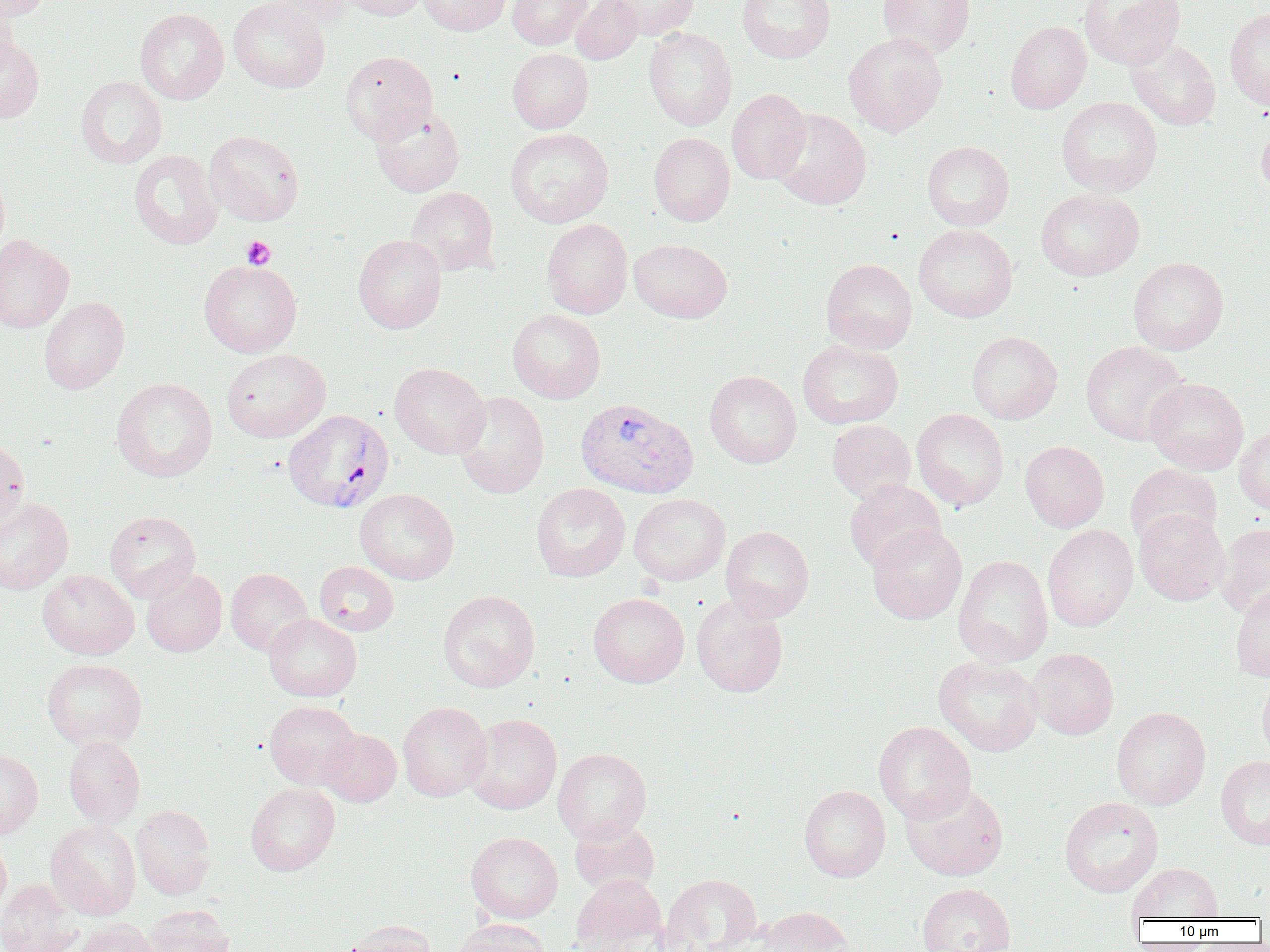

slide_level_diagnosis: Plasmodium vivax
magnification: 1000x
platelet_locations: 'approximate bounding boxes as (x1,y1)-(x2,y2) corner pairs in pixels: (242,235)-(276,270)'
modality: light microscopy
image_size: 1270×952 pixels
preparation: thin blood film
field_of_view: one of a larger specimen
uninfected_red_blood_cell_locations: 'approximate bounding boxes as (x1,y1)-(x2,y2) corner pairs in pixels: (0,0)-(50,20), (229,0)-(330,93), (262,0)-(356,23), (338,0)-(426,21), (419,0)-(510,36), (507,0)-(591,50), (570,0)-(643,65), (612,0)-(699,39), (737,0)-(835,63), (877,0)-(976,58), (1079,0)-(1186,69), (0,3)-(20,79), (1224,7)-(1270,109), (135,8)-(229,104), (1005,21)-(1092,114), (643,27)-(737,130), (843,32)-(947,136), (0,36)-(45,124), (1126,39)-(1221,130), (507,48)-(593,133), (340,50)-(437,144), (75,75)-(167,168), (726,88)-(811,184), (1056,95)-(1161,196), (370,105)-(465,197), (770,108)-(872,209), (1256,119)-(1270,201), (504,127)-(614,227), (204,129)-(305,226), (649,132)-(735,226), (922,140)-(1014,231), (129,149)-(223,250), (0,165)-(10,260), (405,186)-(500,275), (1036,188)-(1145,281), (542,218)-(632,318), (913,224)-(1017,322), (353,234)-(447,333), (0,235)-(74,333), (629,239)-(731,323), (1128,257)-(1228,355), (821,258)-(917,353), (199,259)-(302,358), (39,296)-(129,394), (507,308)-(605,403), (966,330)-(1062,424), (797,339)-(903,429), (1081,341)-(1190,445), (221,349)-(331,442), (390,362)-(490,459), (704,370)-(801,467), (111,377)-(218,482), (1145,378)-(1248,475), (454,391)-(549,498), (912,408)-(1009,510), (827,419)-(915,502), (1235,423)-(1270,514), (0,438)-(29,528), (1020,440)-(1109,532), (1125,464)-(1222,549), (844,479)-(946,572), (531,483)-(630,582), (355,488)-(459,585), (629,493)-(730,585), (0,497)-(74,594), (1134,509)-(1229,605), (105,510)-(201,602), (1217,522)-(1270,616), (867,524)-(967,624), (1042,524)-(1138,631), (720,525)-(814,622), (953,555)-(1053,666), (314,561)-(399,636), (141,568)-(227,657), (225,568)-(312,656), (37,569)-(139,659), (1230,583)-(1270,681), (438,589)-(539,692), (588,593)-(689,688), (691,595)-(788,697), (263,613)-(362,701), (1028,648)-(1119,739), (933,654)-(1044,756), (42,658)-(147,750), (1257,676)-(1270,766), (264,700)-(360,789), (397,701)-(492,801), (1111,706)-(1211,810), (464,713)-(562,814), (873,721)-(975,822), (318,728)-(401,806), (63,735)-(145,827), (0,748)-(43,840), (553,748)-(651,843), (1215,755)-(1270,850), (900,781)-(1009,881), (245,782)-(340,876), (799,784)-(890,882), (1059,796)-(1163,897), (131,804)-(216,899), (569,816)-(660,896), (45,819)-(141,920), (466,832)-(563,923), (0,838)-(11,915), (1126,862)-(1223,921), (570,874)-(667,951), (659,874)-(762,951), (0,880)-(83,952), (916,882)-(1016,952), (142,904)-(234,952), (753,905)-(854,952), (450,918)-(551,952), (74,919)-(157,952), (339,920)-(438,952)'
plasmodium_vivax_infected_red_blood_cell_locations: 'approximate bounding boxes as (x1,y1)-(x2,y2) corner pairs in pixels: (575,396)-(699,498), (283,409)-(394,513)'